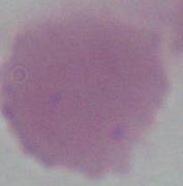

{
  "magnification": "1000x",
  "identification": "red blood cell",
  "modality": "photomicrograph"
}